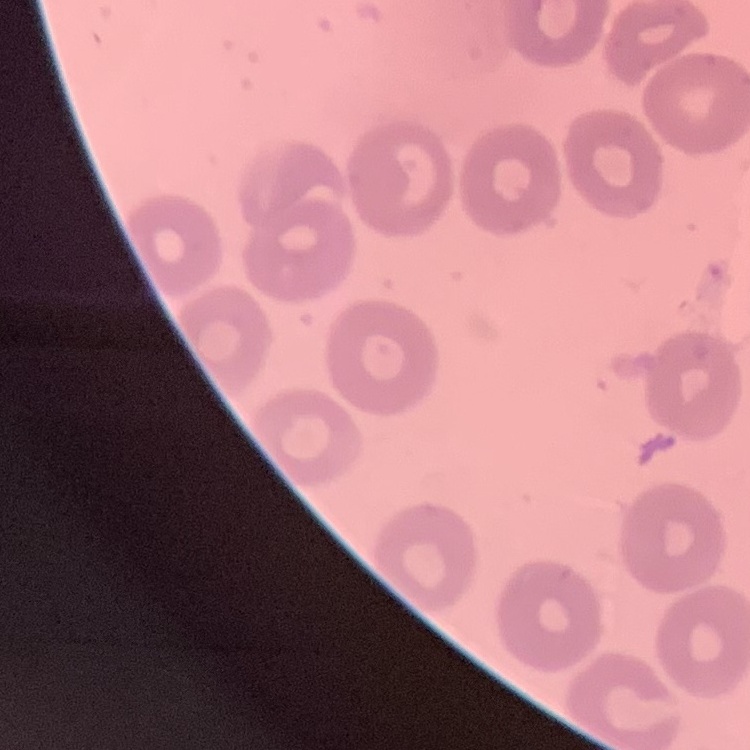
{
  "erythrocyte_morphology": "no rouleaux formation",
  "preparation": "thin blood smear",
  "stain": "Field's or Giemsa",
  "image_type": "one tile cut from a larger photomicrograph"
}